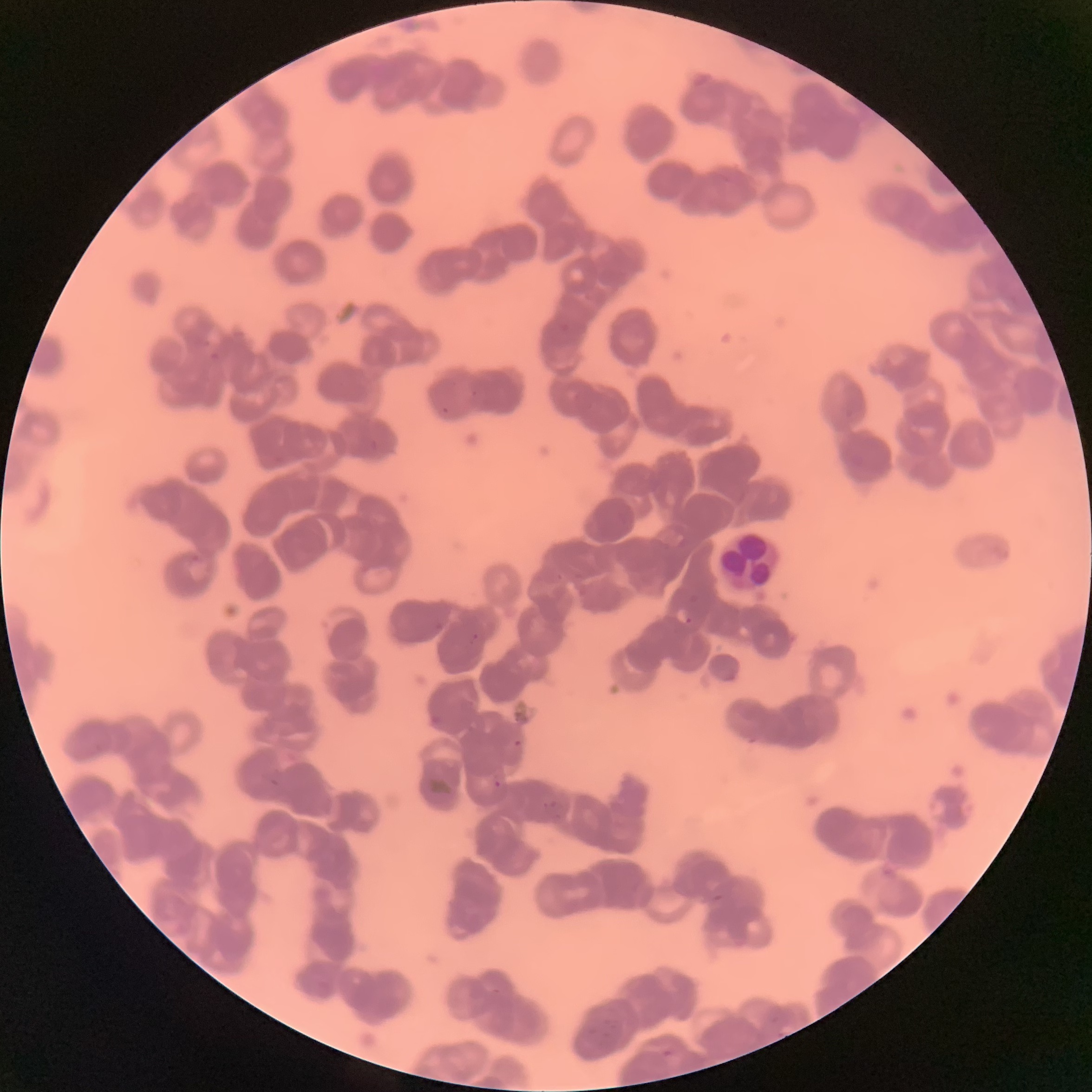

Approximate bounding boxes as (x1, y1, x2, y2) in pixels. White blood cell locations: (720, 533, 780, 590). Plasmodium parasite locations: (208, 351, 221, 361), (676, 608, 692, 626), (469, 632, 479, 646), (428, 713, 439, 725), (513, 737, 522, 747), (270, 776, 281, 789), (493, 779, 502, 789), (491, 988, 502, 995), (663, 1049, 672, 1059). The red blood cells show rouleaux formation. Optical microscopy. Thin blood film. Image is 1092×1092 pixels.